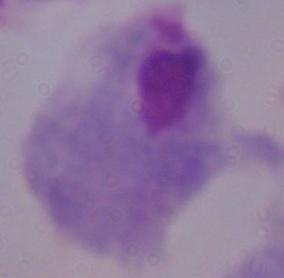

A trichomonad is seen. Micrograph. 1000x magnification.